Describe the morphology of the erythrocytes.
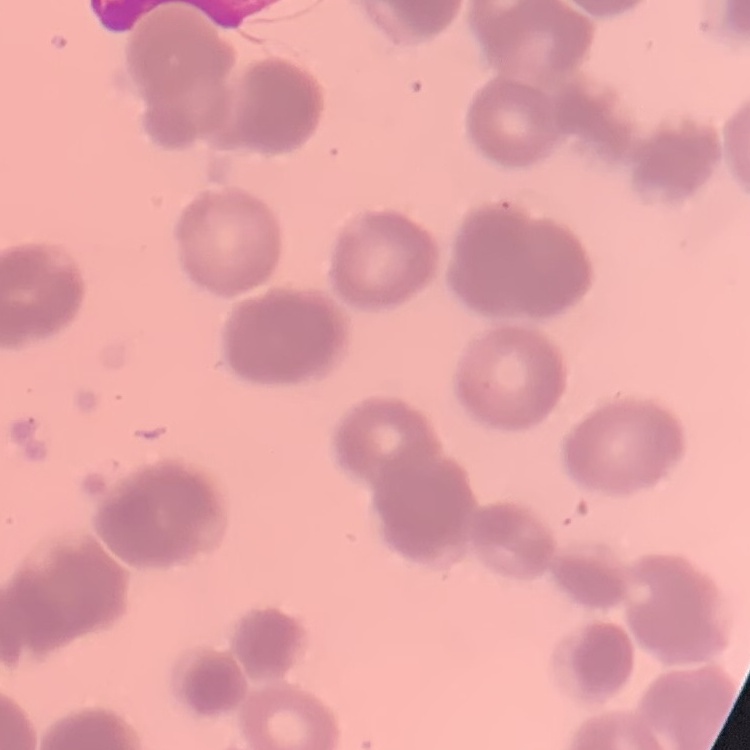
Rouleaux formation.

Summary:
  - Image type: one tile cut from a larger photomicrograph
  - Stain: Field's or Giemsa
  - Preparation: thin blood film